Describe the morphology of the erythrocytes.
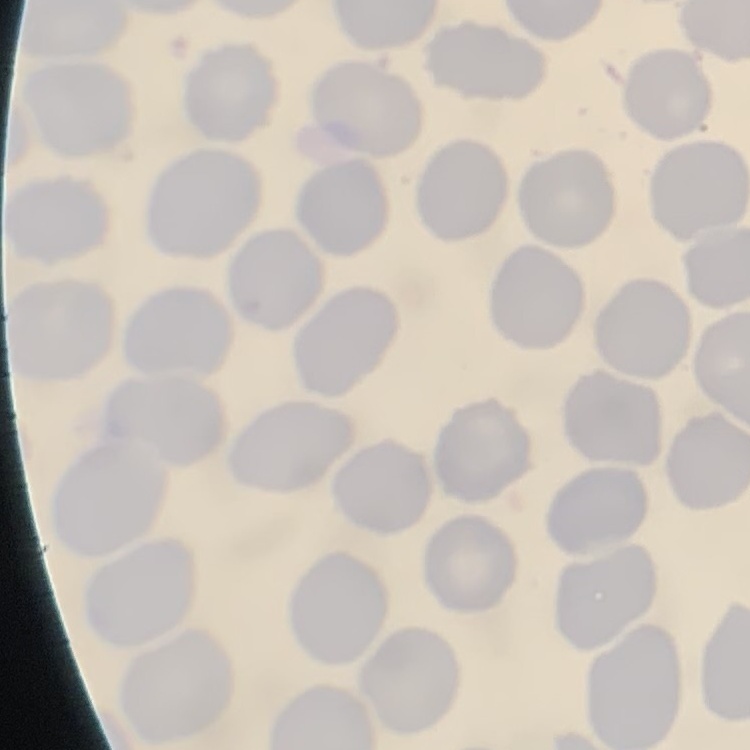

They show no rouleaux formation.

image_type: square crop of a larger photomicrograph
preparation: thin peripheral smear
stain: Field's or Giemsa